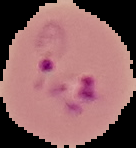

Summary:
  - Preparation: thin blood smear
  - Image type: cell region segmented out of the field of view; surrounding area masked to black
  - Image size: 136×148 pixels
  - Malaria status: parasitized